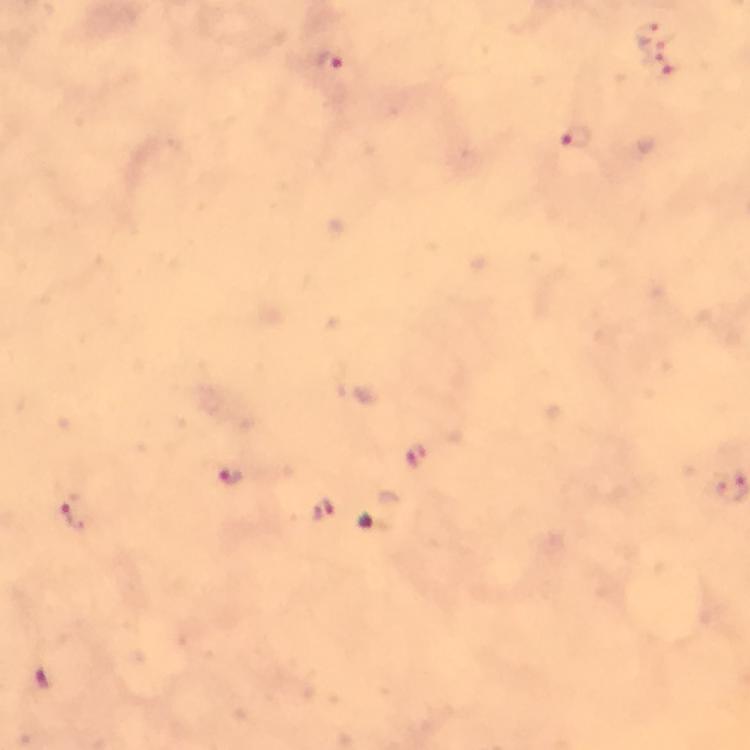
Plasmodium parasite locations = approximate centers as (x, y) in pixels: (647, 31), (331, 62), (659, 64), (576, 138), (415, 455), (232, 475), (320, 511), (74, 513), (48, 680)
stain = Giemsa
magnification = 100x
context = from a diagnostic examination for malaria
image size = 750×750 pixels
capture = smartphone mounted on the microscope
immersion oil = used
preparation = thick blood film
cropped from = a single field of view